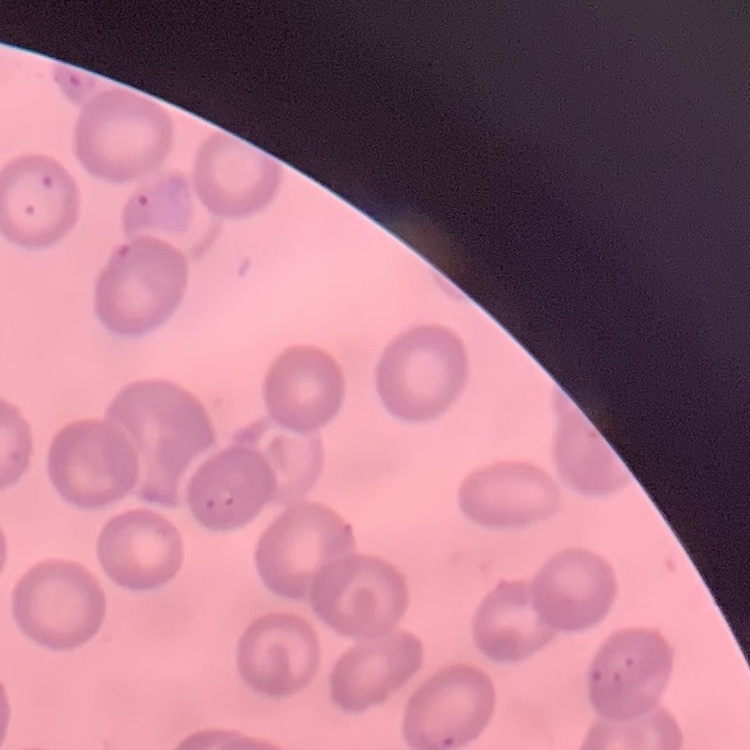
{
  "red_blood_cell_morphology": "no rouleaux formation",
  "stain": "Field's or Giemsa",
  "image_type": "one tile cut from a larger photomicrograph",
  "preparation": "thin blood smear"
}